Comment on the morphology of the red blood cells.
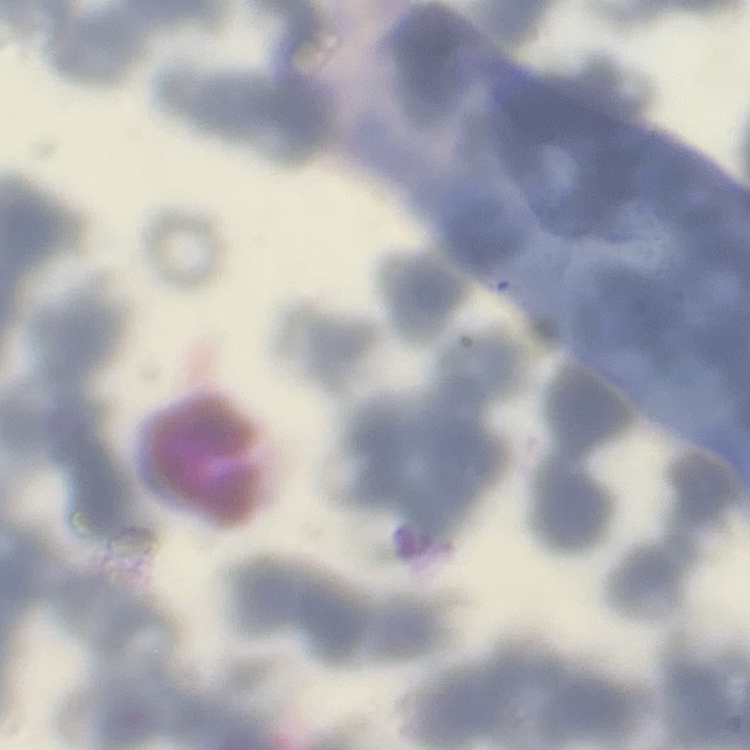

They show rouleaux formation.

{
  "stain": "Field's or Giemsa",
  "image_type": "square crop of a larger photomicrograph",
  "preparation": "thin blood film"
}